Classify this cell by malaria status.
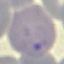
It is parasitized.

{
  "capture": "smartphone through the microscope eyepiece",
  "image_type": "automatically extracted cell patch, resized to 64 × 64 pixels",
  "preparation": "thin blood film",
  "stain": "Giemsa"
}